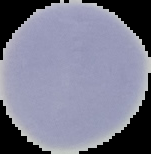

Summary:
  - Result: no Plasmodium parasites detected
  - Preparation: thin blood film
  - Image size: 151×154 pixels
  - Image type: cell region segmented out of the field of view; surrounding area masked to black